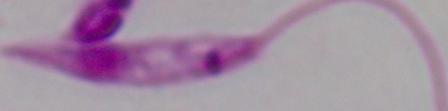
A Leishmania parasite is seen. Photomicrograph. Captured at 1000x magnification.